Evaluate for malaria.
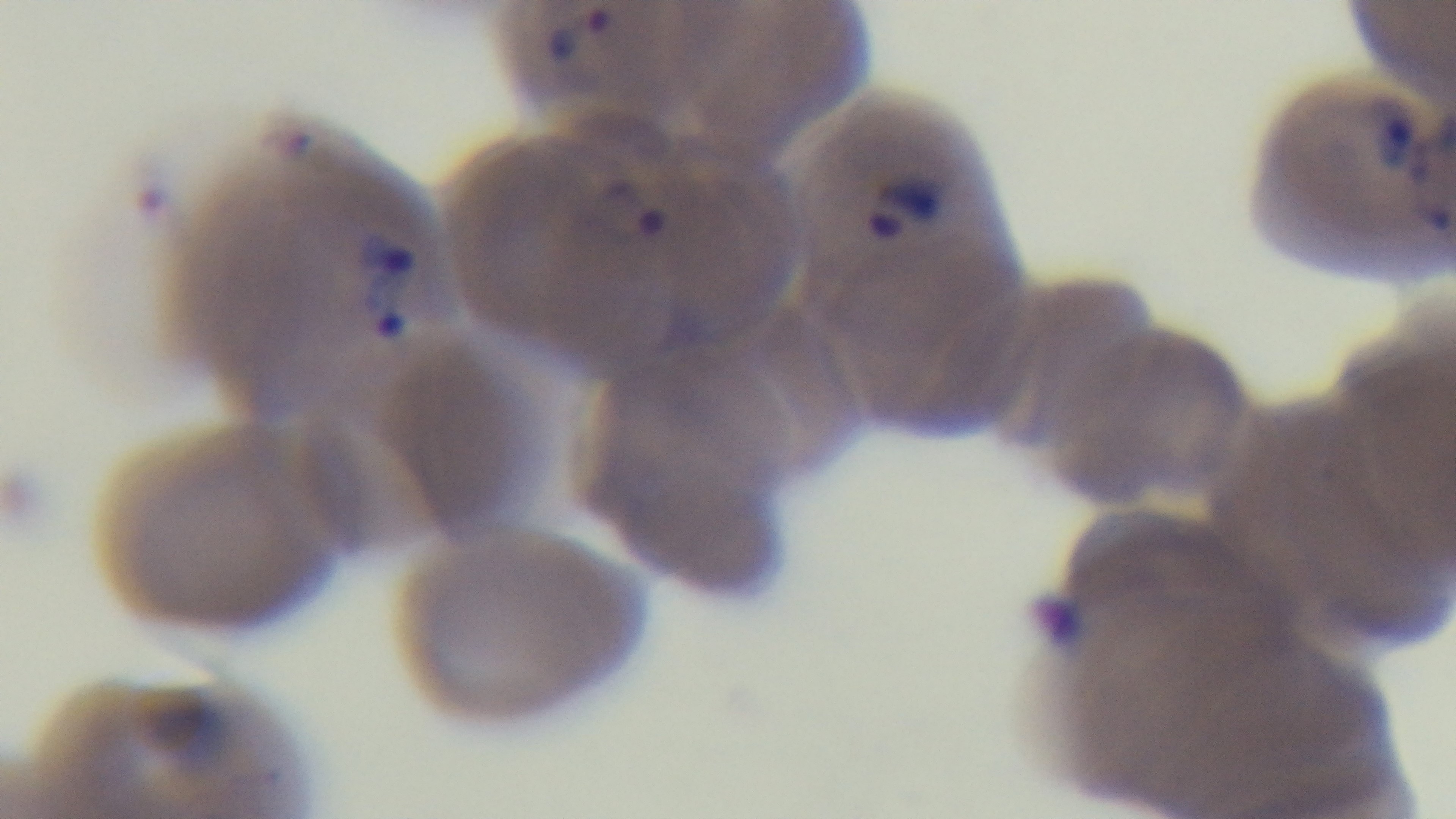
Positive.

Summary:
  - Capture: mounted 4K digital camera
  - Stain: Giemsa
  - Objective: 100x oil immersion
  - Field of view: one from the slide
  - Preparation: thin blood film
  - Modality: light microscopy